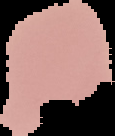

Summary:
  - Image size: 115×136 pixels
  - Malaria status: uninfected
  - Preparation: thin blood smear
  - Image type: segmented cell region with the area outside set to black